Assess the morphology of the erythrocytes.
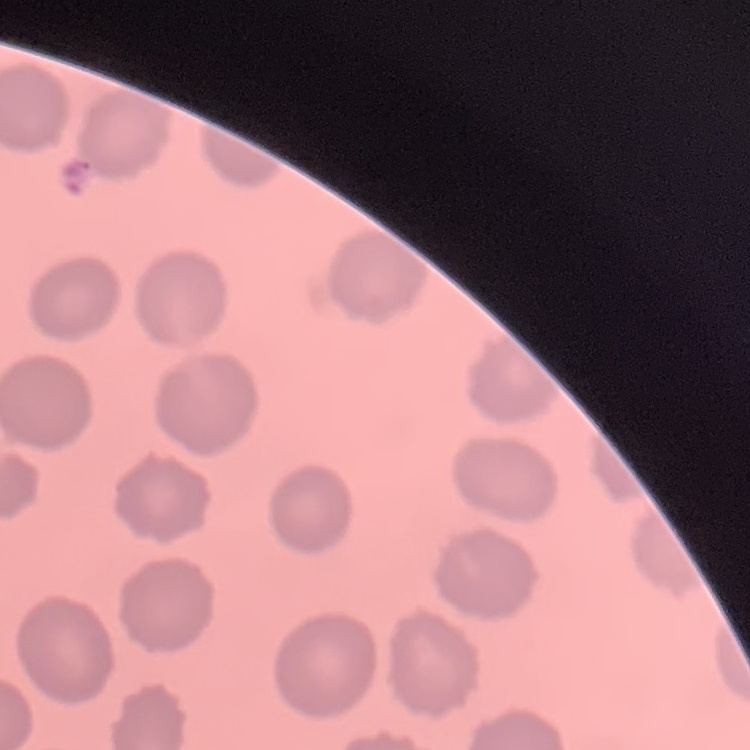
They show no rouleaux formation.

One tile cut from a larger photomicrograph. Thin peripheral smear. Stained with either Field's or Giemsa.